Assess this cell for malaria.
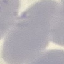
It is uninfected.

Thin blood smear. Acquired by smartphone through the microscope eyepiece. Cell patch, automatically extracted from a larger field of view and resized to 64 × 64 pixels. Giemsa-stained preparation.